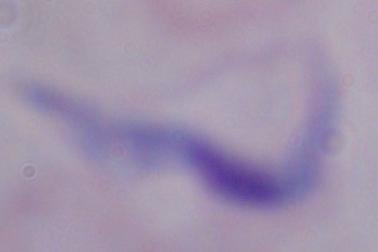

Photomicrograph. A trypanosome is seen. Captured at 1000x magnification.